State the preparation type.
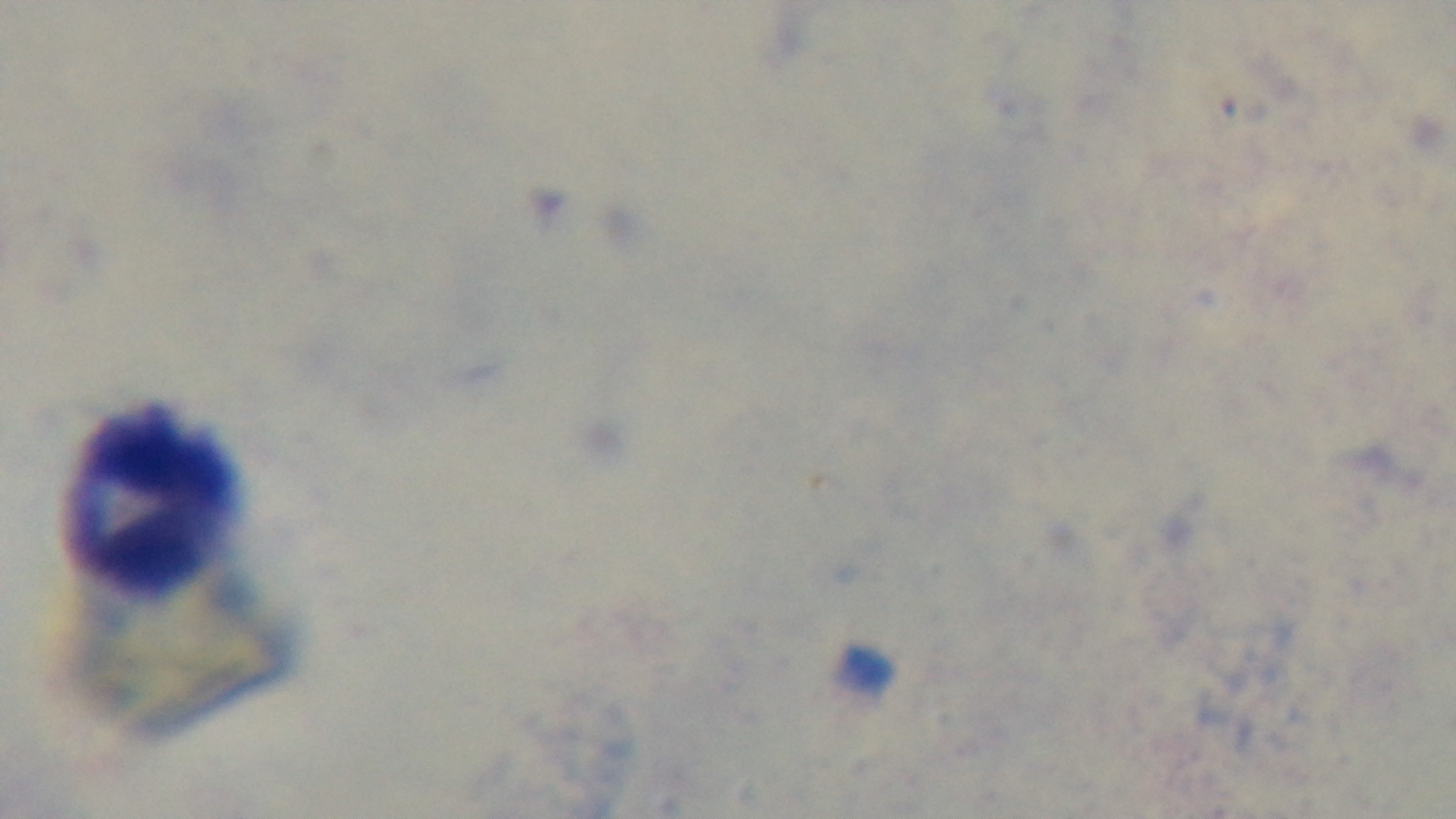

A thick smear.

Photomicrograph. Malaria status: uninfected. 100x oil-immersion objective. Captured with a mounted 4K digital camera. One field from the slide. Giemsa stain.